Give the extent of all uninfected red blood cells.
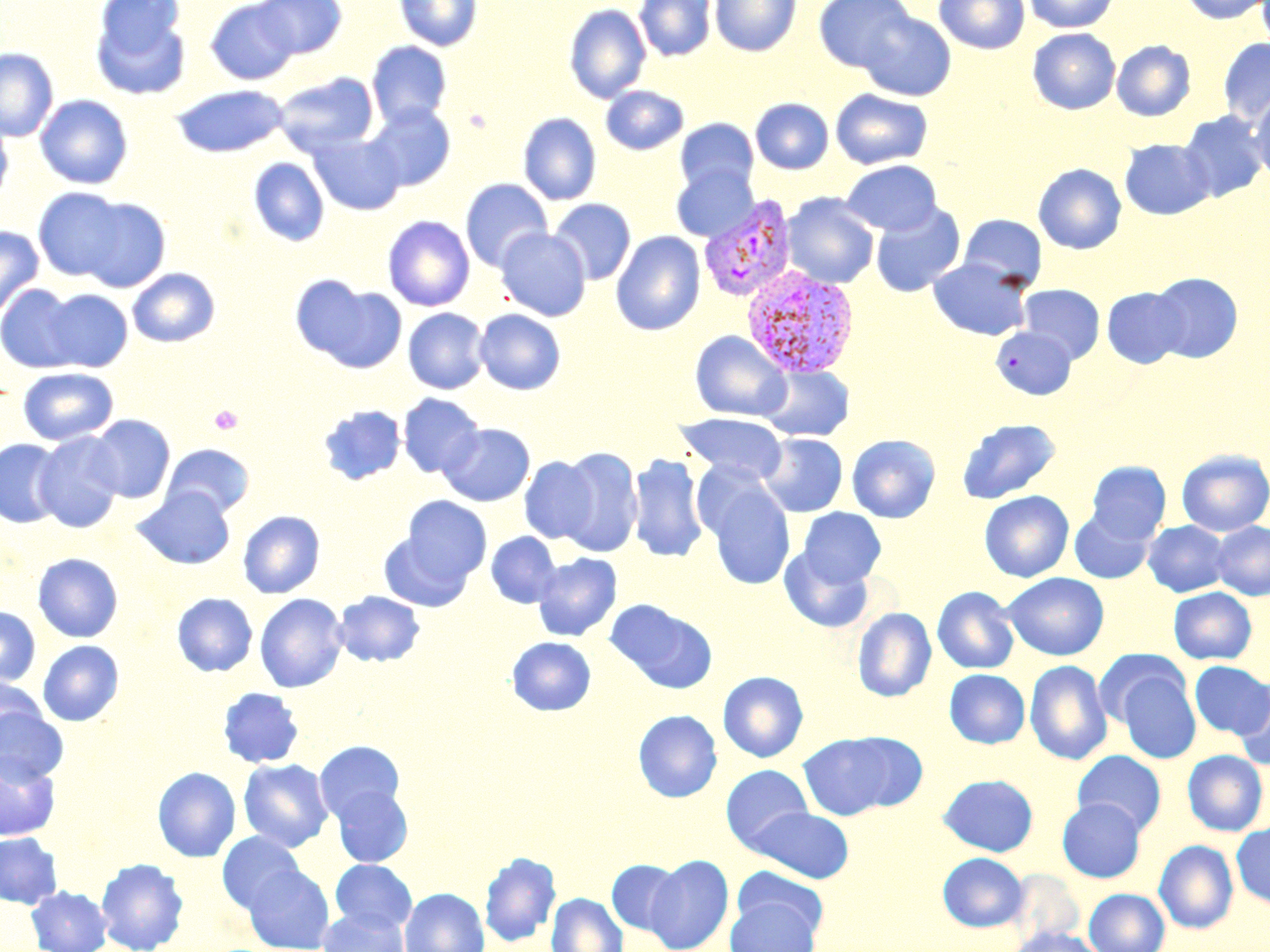
Approximate bounding boxes as named x1/y1/x2/y2 corners in pixels.
Uninfected red blood cells: (x1=205, y1=0, x2=301, y2=85), (x1=254, y1=0, x2=347, y2=59), (x1=394, y1=0, x2=482, y2=51), (x1=634, y1=0, x2=717, y2=61), (x1=709, y1=0, x2=801, y2=56), (x1=813, y1=0, x2=915, y2=72), (x1=934, y1=0, x2=1030, y2=54), (x1=1023, y1=0, x2=1120, y2=33), (x1=1181, y1=0, x2=1269, y2=24), (x1=89, y1=1, x2=192, y2=100), (x1=564, y1=4, x2=651, y2=103), (x1=858, y1=11, x2=956, y2=100), (x1=1027, y1=29, x2=1120, y2=114), (x1=1218, y1=38, x2=1270, y2=126), (x1=1112, y1=40, x2=1196, y2=121), (x1=366, y1=41, x2=452, y2=127), (x1=0, y1=48, x2=58, y2=141), (x1=274, y1=71, x2=379, y2=157), (x1=172, y1=84, x2=289, y2=158), (x1=600, y1=86, x2=689, y2=154), (x1=830, y1=89, x2=933, y2=170), (x1=1250, y1=91, x2=1270, y2=182), (x1=35, y1=95, x2=133, y2=189), (x1=750, y1=98, x2=833, y2=174), (x1=365, y1=103, x2=456, y2=191), (x1=1179, y1=110, x2=1269, y2=202), (x1=0, y1=113, x2=12, y2=207), (x1=518, y1=113, x2=601, y2=205), (x1=675, y1=118, x2=759, y2=196), (x1=308, y1=132, x2=406, y2=216), (x1=1120, y1=138, x2=1214, y2=220), (x1=248, y1=157, x2=329, y2=247), (x1=841, y1=159, x2=942, y2=235), (x1=1033, y1=163, x2=1126, y2=254), (x1=671, y1=164, x2=758, y2=243), (x1=460, y1=178, x2=553, y2=272), (x1=33, y1=188, x2=128, y2=281), (x1=782, y1=193, x2=880, y2=289), (x1=76, y1=198, x2=171, y2=292), (x1=548, y1=198, x2=636, y2=285), (x1=870, y1=203, x2=965, y2=297), (x1=958, y1=214, x2=1047, y2=290), (x1=382, y1=216, x2=475, y2=311), (x1=0, y1=226, x2=44, y2=320), (x1=496, y1=227, x2=591, y2=321), (x1=611, y1=231, x2=705, y2=336), (x1=927, y1=258, x2=1033, y2=340), (x1=128, y1=268, x2=220, y2=347), (x1=1148, y1=272, x2=1243, y2=363), (x1=293, y1=277, x2=407, y2=373), (x1=1, y1=284, x2=82, y2=372), (x1=1018, y1=284, x2=1105, y2=363), (x1=1102, y1=287, x2=1188, y2=368), (x1=41, y1=289, x2=132, y2=372), (x1=402, y1=307, x2=490, y2=394), (x1=474, y1=308, x2=566, y2=395), (x1=991, y1=326, x2=1077, y2=400), (x1=690, y1=331, x2=791, y2=421), (x1=759, y1=365, x2=854, y2=442), (x1=17, y1=367, x2=119, y2=446), (x1=397, y1=393, x2=484, y2=478), (x1=318, y1=405, x2=406, y2=485), (x1=675, y1=412, x2=789, y2=484), (x1=86, y1=415, x2=175, y2=503), (x1=955, y1=418, x2=1062, y2=504), (x1=439, y1=423, x2=535, y2=506), (x1=34, y1=431, x2=124, y2=533), (x1=759, y1=433, x2=847, y2=517), (x1=846, y1=434, x2=940, y2=522), (x1=0, y1=438, x2=65, y2=529), (x1=161, y1=442, x2=254, y2=518), (x1=556, y1=446, x2=643, y2=558), (x1=1176, y1=449, x2=1270, y2=536), (x1=627, y1=453, x2=709, y2=563), (x1=519, y1=456, x2=598, y2=544), (x1=1086, y1=461, x2=1171, y2=542), (x1=703, y1=479, x2=796, y2=590), (x1=132, y1=487, x2=235, y2=569), (x1=979, y1=491, x2=1074, y2=582), (x1=400, y1=496, x2=492, y2=584), (x1=798, y1=508, x2=886, y2=586), (x1=1068, y1=508, x2=1155, y2=584), (x1=238, y1=511, x2=325, y2=598), (x1=244, y1=511, x2=340, y2=684), (x1=1144, y1=521, x2=1230, y2=596), (x1=1211, y1=521, x2=1270, y2=599), (x1=378, y1=529, x2=474, y2=612), (x1=486, y1=532, x2=561, y2=608), (x1=779, y1=547, x2=874, y2=632), (x1=533, y1=552, x2=622, y2=641), (x1=33, y1=553, x2=123, y2=642), (x1=1003, y1=572, x2=1109, y2=660), (x1=932, y1=586, x2=1019, y2=674), (x1=1169, y1=587, x2=1256, y2=664), (x1=1181, y1=587, x2=1262, y2=737), (x1=333, y1=591, x2=426, y2=667), (x1=172, y1=593, x2=258, y2=677), (x1=254, y1=593, x2=348, y2=692), (x1=605, y1=599, x2=717, y2=693), (x1=0, y1=607, x2=40, y2=686), (x1=852, y1=607, x2=936, y2=702), (x1=507, y1=637, x2=596, y2=716), (x1=38, y1=640, x2=124, y2=726), (x1=1096, y1=650, x2=1188, y2=728), (x1=1025, y1=660, x2=1112, y2=765), (x1=1189, y1=661, x2=1269, y2=738), (x1=1113, y1=667, x2=1200, y2=764), (x1=944, y1=669, x2=1029, y2=748), (x1=718, y1=671, x2=808, y2=762), (x1=0, y1=676, x2=48, y2=747), (x1=1233, y1=680, x2=1270, y2=771), (x1=218, y1=687, x2=305, y2=768), (x1=0, y1=708, x2=67, y2=783), (x1=633, y1=710, x2=722, y2=802), (x1=799, y1=732, x2=903, y2=820), (x1=315, y1=741, x2=405, y2=824), (x1=1182, y1=750, x2=1268, y2=836), (x1=1072, y1=751, x2=1166, y2=835), (x1=0, y1=754, x2=59, y2=840), (x1=238, y1=758, x2=333, y2=852), (x1=721, y1=765, x2=814, y2=850), (x1=152, y1=767, x2=240, y2=862), (x1=938, y1=774, x2=1038, y2=856), (x1=330, y1=784, x2=413, y2=868), (x1=1057, y1=798, x2=1146, y2=882), (x1=746, y1=806, x2=854, y2=883), (x1=1232, y1=823, x2=1270, y2=907), (x1=0, y1=832, x2=62, y2=908), (x1=218, y1=832, x2=306, y2=914), (x1=1154, y1=840, x2=1238, y2=933), (x1=479, y1=851, x2=561, y2=947), (x1=937, y1=853, x2=1028, y2=932), (x1=645, y1=854, x2=733, y2=952), (x1=96, y1=858, x2=189, y2=952), (x1=606, y1=859, x2=684, y2=935), (x1=330, y1=860, x2=417, y2=933), (x1=243, y1=864, x2=334, y2=952), (x1=732, y1=866, x2=828, y2=940), (x1=1005, y1=870, x2=1084, y2=945), (x1=27, y1=886, x2=111, y2=952), (x1=399, y1=887, x2=489, y2=952), (x1=1084, y1=889, x2=1169, y2=952), (x1=547, y1=893, x2=627, y2=952), (x1=726, y1=898, x2=820, y2=952), (x1=317, y1=908, x2=409, y2=952), (x1=1007, y1=926, x2=1104, y2=952).

slide-level diagnosis = Plasmodium vivax
image size = 1270×952 pixels
field of view = single
stain = May-Grünwald-Giemsa
magnification = 1000x
modality = optical microscopy
preparation = thin blood smear
Plasmodium vivax-infected red blood cell locations = approximate bounding boxes as named x1/y1/x2/y2 corners in pixels: (x1=698, y1=196, x2=797, y2=302), (x1=742, y1=267, x2=860, y2=379)
platelet locations = approximate bounding boxes as named x1/y1/x2/y2 corners in pixels: (x1=209, y1=405, x2=243, y2=436)